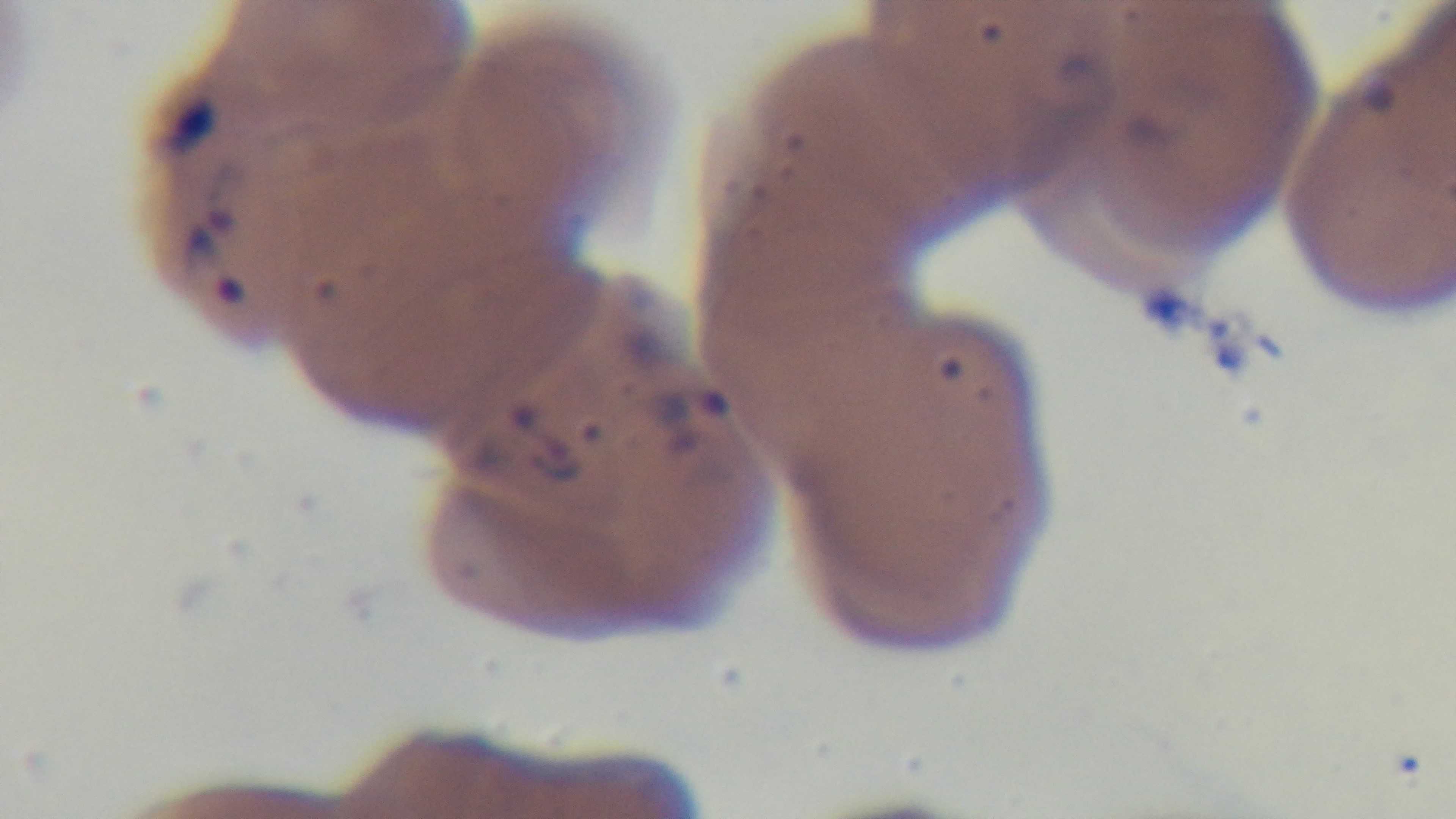 Light microscopy. Malaria status: infected. Single field of view. Preparation: thin smear. Mounted 4K digital camera. 100x oil-immersion objective. Giemsa stain.